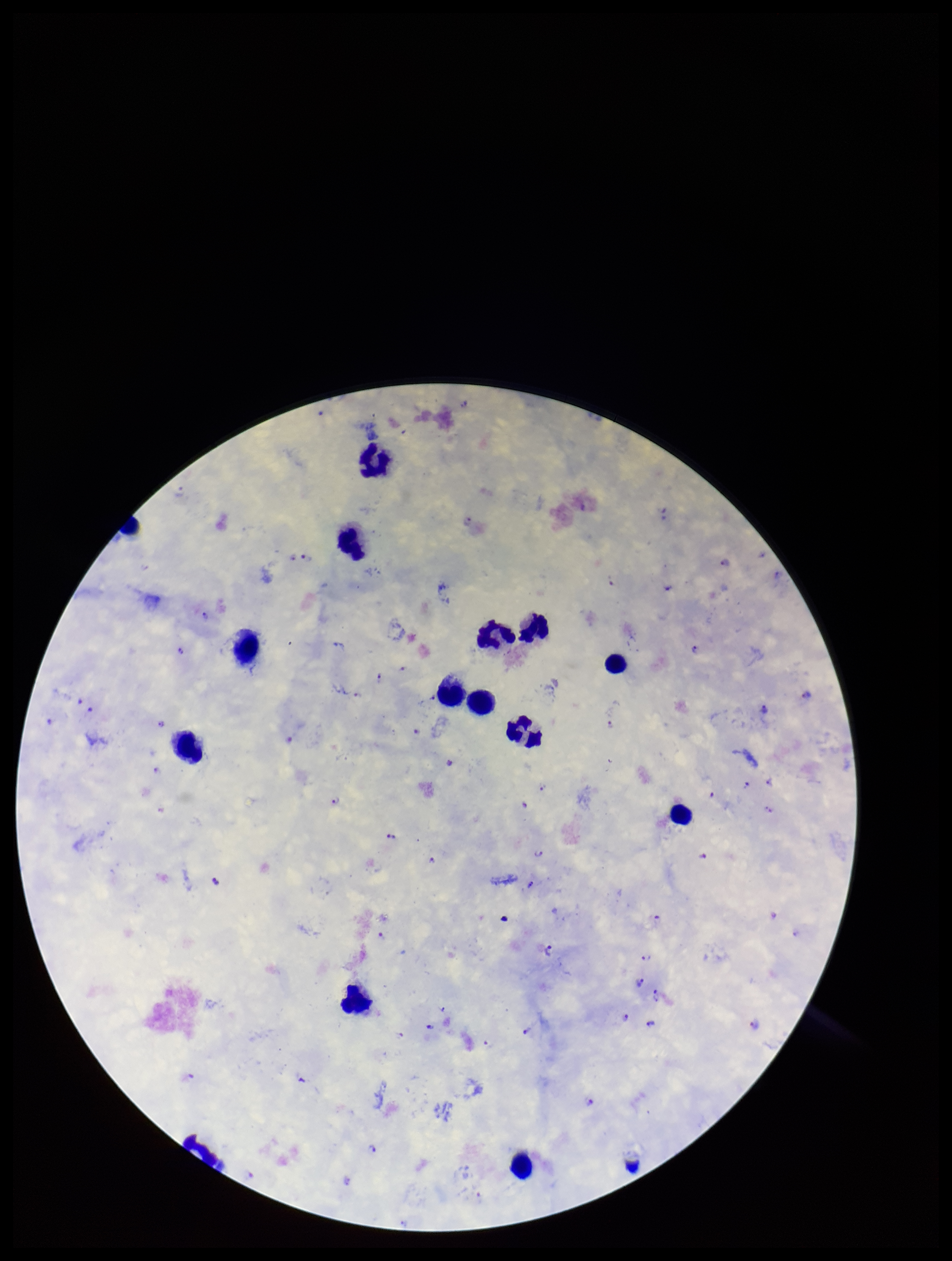
preparation = thick blood smear
stain = Giemsa
leukocyte count = 13
species reported for this patient = Plasmodium falciparum
field of view = one from this slide
capture = smartphone photograph through the microscope eyepiece
image size = 952×1261 pixels
Plasmodium parasites = detected
parasite count = 49
patient malaria status = positive